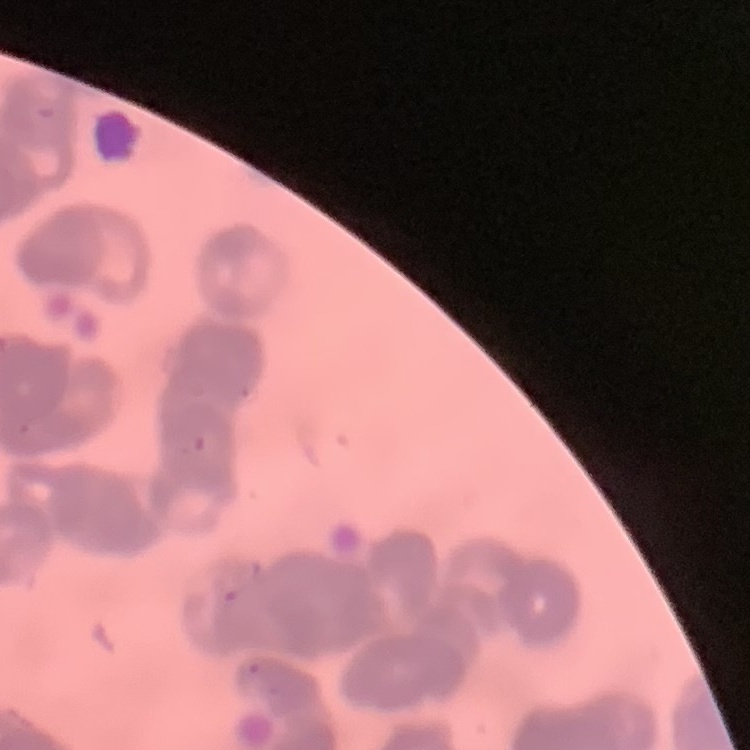

The erythrocytes show rouleaux formation. Thin blood smear. Square crop of a larger photomicrograph. Stained with either Field's or Giemsa.